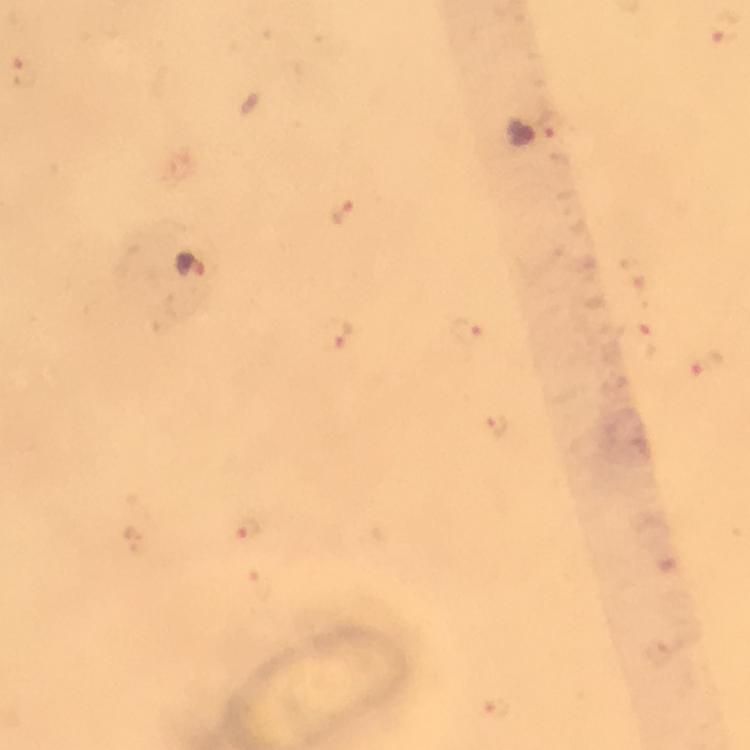
Approximate centers as (x, y) in pixels. Malaria parasite locations: (726, 35), (25, 71), (548, 129), (521, 131), (342, 211), (192, 265), (470, 332), (337, 334), (639, 340), (705, 365), (496, 428), (246, 528), (497, 708). From a diagnostic examination for malaria. At 100x magnification. Cropped region of a single field of view. Photographed through the microscope with a smartphone camera. Immersion oil was used. Image is 750×750 pixels. Giemsa-stained preparation. Thick blood film.